State which cell type is depicted.
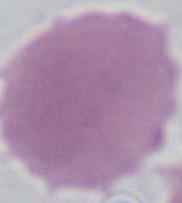

An erythrocyte.

magnification = 1000x
modality = micrograph